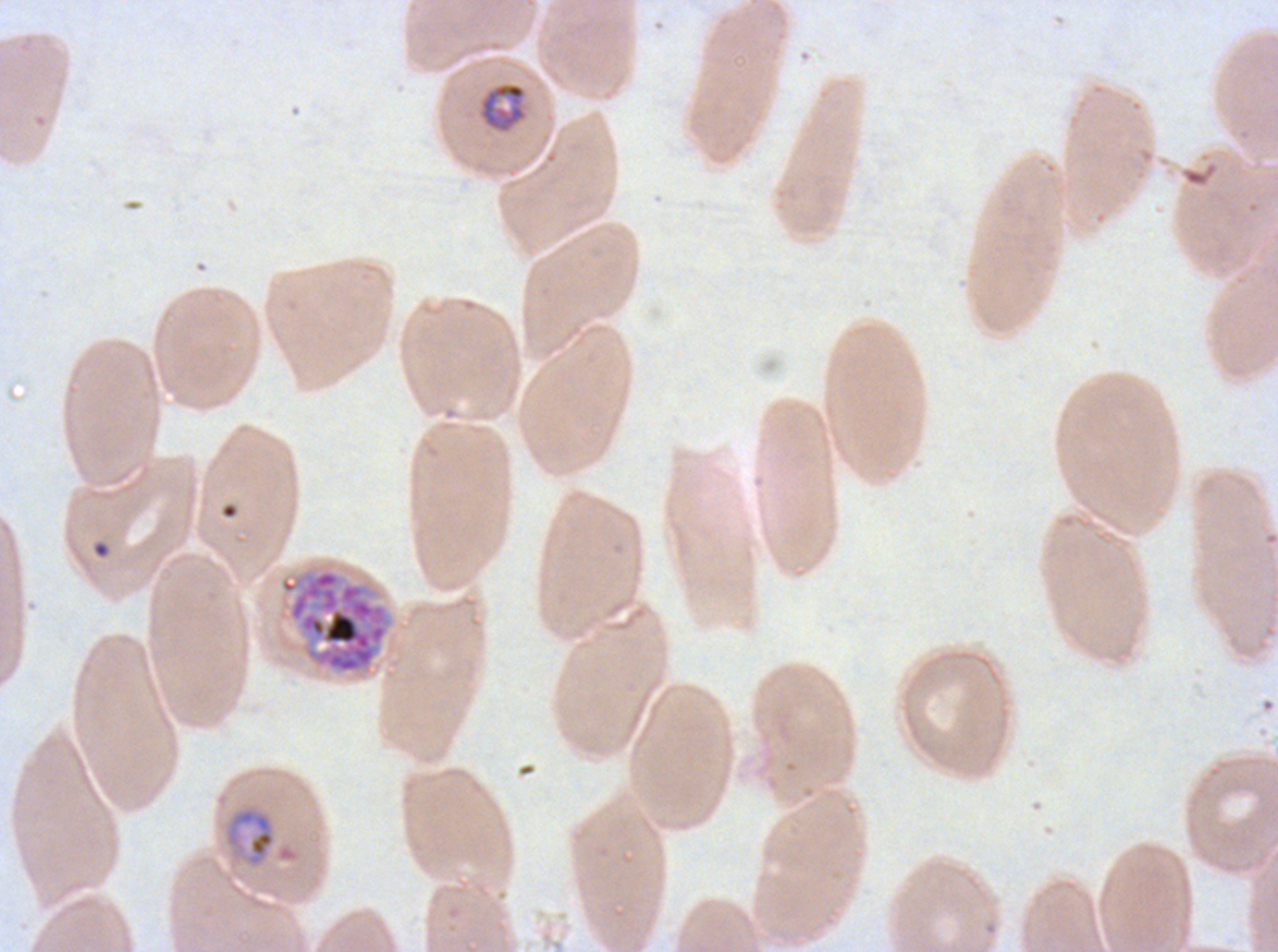 Approximate bounding boxes as {x1, y1, x2, y2} in pixels. Ring locations: {221, 503, 238, 519}, {92, 541, 110, 559}. Mid trophozoite locations: {480, 82, 526, 132}, {224, 805, 276, 868}. Late schizont locations: {278, 568, 393, 675}. Life-cycle stages observed: ring, mid trophozoite, late schizont. Giemsa-stained preparation. P. falciparum from a patient in The Gambia, cultured ex vivo for 24 to 48 hours. Image is 1278×952 pixels. Thin blood film. A sub-image separated from a larger composite.